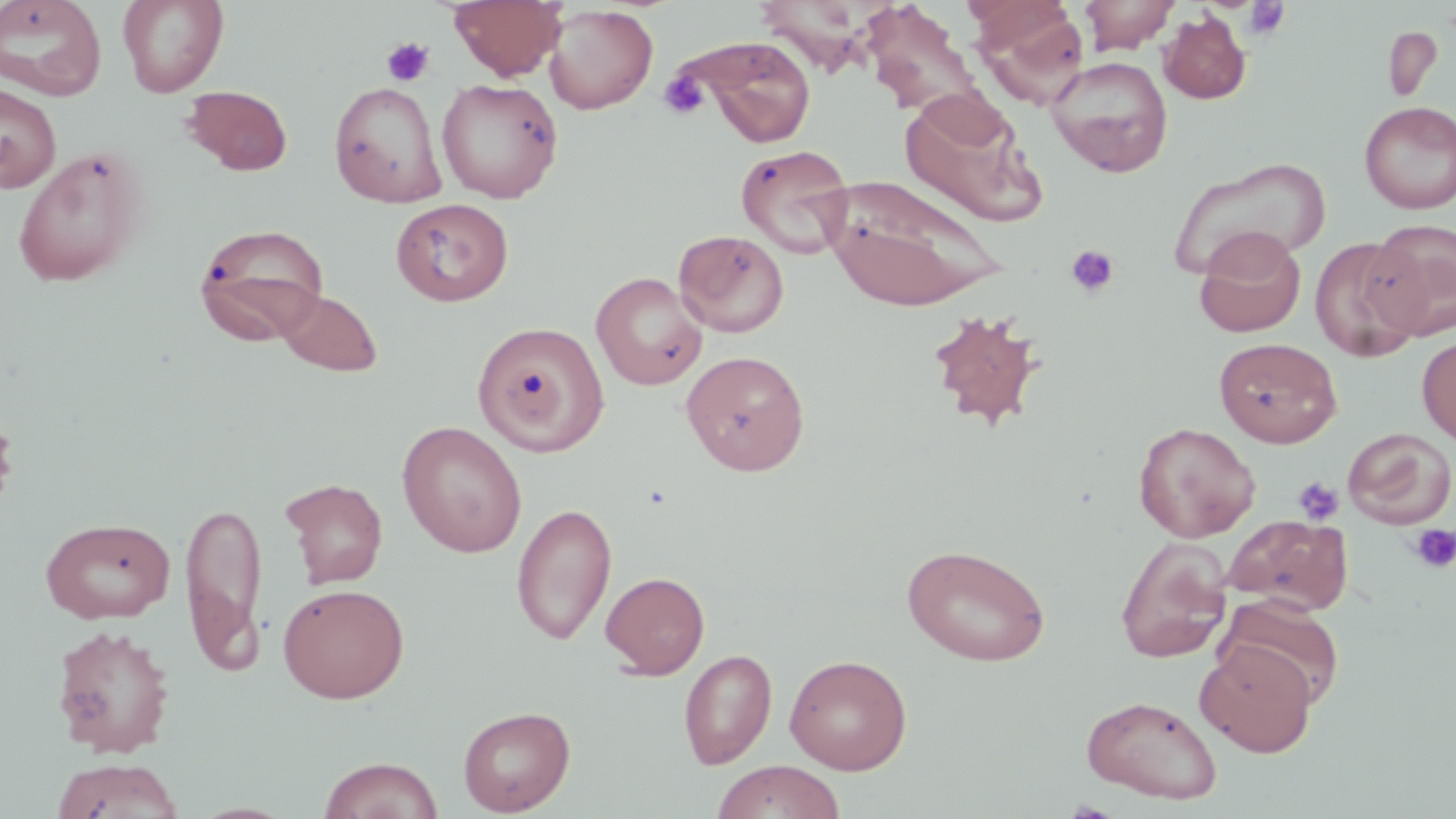
Summary:
  - Coordinate format: approximate bounding boxes as (x1, y1, x2, y2) in pixels
  - Uninfected red blood cell locations: (0, 0, 107, 101), (117, 0, 229, 98), (449, 0, 567, 81), (1078, 0, 1183, 54), (859, 2, 985, 117), (971, 2, 1090, 107), (544, 4, 658, 114), (1158, 10, 1251, 104), (1382, 25, 1443, 103), (690, 38, 818, 147), (1046, 56, 1173, 177), (437, 78, 563, 203), (329, 80, 447, 207), (0, 82, 61, 193), (182, 85, 293, 176), (898, 90, 1048, 227), (1359, 101, 1456, 213), (735, 144, 855, 259), (13, 146, 150, 288), (1169, 157, 1328, 280), (824, 175, 1006, 312), (390, 197, 514, 307), (1366, 219, 1456, 340), (193, 223, 330, 346), (673, 229, 789, 337), (1195, 230, 1306, 338), (1310, 237, 1424, 362), (591, 271, 708, 391), (276, 289, 383, 377), (925, 308, 1046, 431), (471, 319, 612, 458), (1417, 335, 1456, 446), (1214, 338, 1342, 447), (681, 350, 810, 475), (396, 420, 527, 557), (1133, 422, 1260, 542), (1342, 427, 1456, 529), (280, 477, 388, 589), (179, 498, 269, 674), (511, 502, 618, 646), (1222, 514, 1353, 616), (40, 517, 175, 624), (1116, 536, 1233, 663), (901, 542, 1051, 667), (600, 570, 710, 679), (276, 583, 410, 703), (1217, 596, 1346, 709), (50, 624, 176, 758), (1195, 640, 1318, 757), (679, 648, 777, 770), (785, 654, 912, 774), (1081, 695, 1223, 804), (458, 704, 575, 815), (317, 756, 444, 819), (50, 758, 185, 818), (711, 760, 846, 819)
  - Platelet locations: (1244, 1, 1291, 39), (382, 38, 434, 87), (659, 71, 709, 119), (1064, 245, 1120, 298), (1293, 476, 1343, 526), (1409, 524, 1456, 574)
  - Slide-level diagnosis: negative for blood parasites
  - Preparation: thin blood film
  - Field of view: single
  - Modality: optical microscopy
  - Stain: May-Grünwald-Giemsa
  - Magnification: 1000x
  - Image size: 1456×819 pixels